Report the malaria status of this cell.
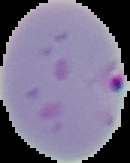

It is parasitized.

From a thin blood smear. Segmented cell region on a black background. Image is 130×163 pixels.